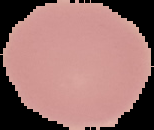

Summary:
  - Malaria status: uninfected
  - Image size: 154×130 pixels
  - Preparation: thin blood film
  - Image type: cell region segmented out of the field of view; surrounding area masked to black